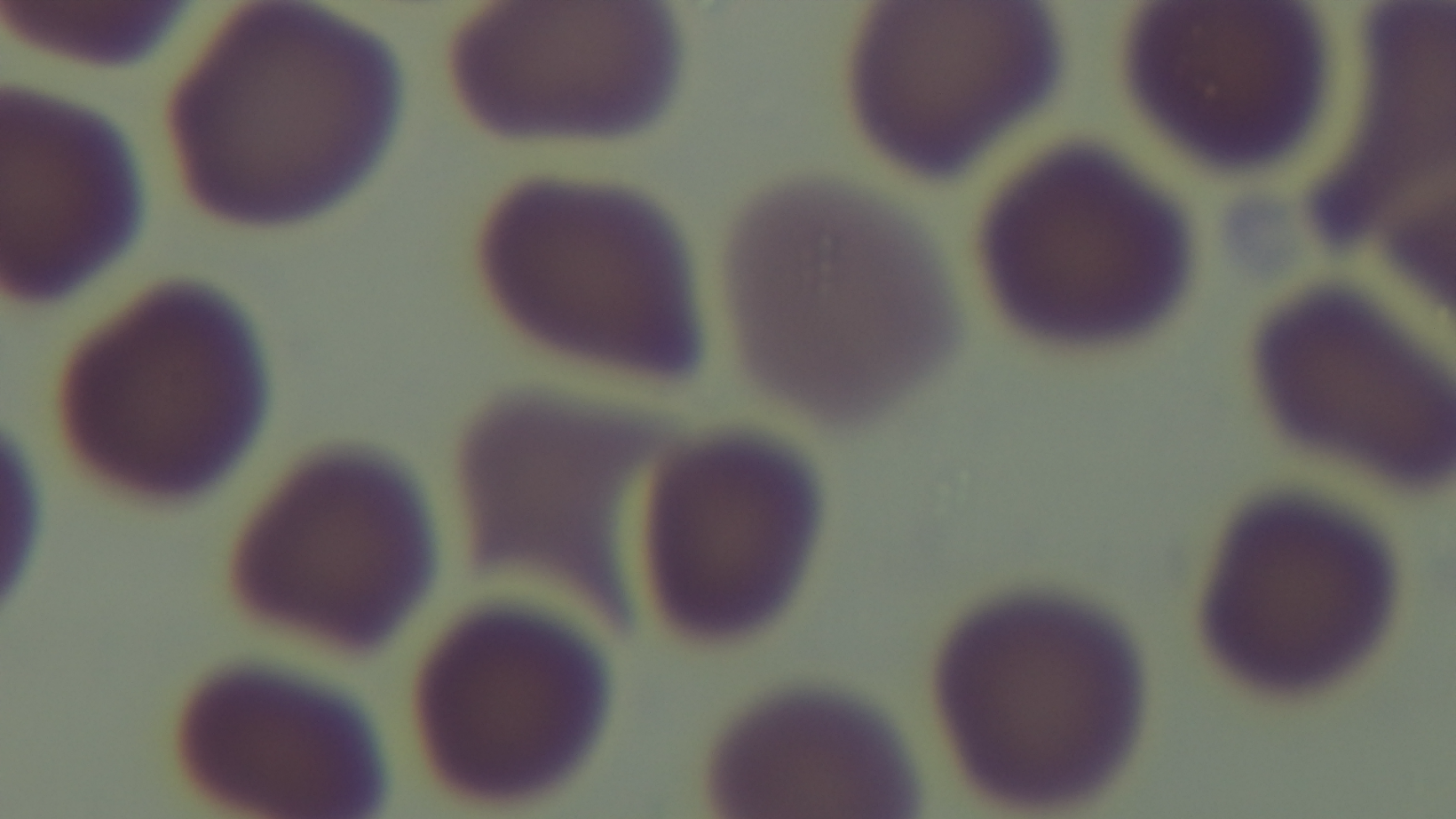

Single field of view. Preparation: thin blood film. Malaria status: uninfected. Light microscopy. Giemsa stain. Mounted 4K digital camera. Oil-immersion objective, 100x.